Assess this cell for malaria.
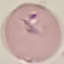

Parasitized.

Summary:
  - Image type: cell patch, automatically extracted from a larger field of view and resized to 64 × 64 pixels
  - Capture: smartphone through the microscope eyepiece
  - Preparation: thin blood film
  - Stain: Giemsa